Locate every Plasmodium vivax-infected red blood cell.
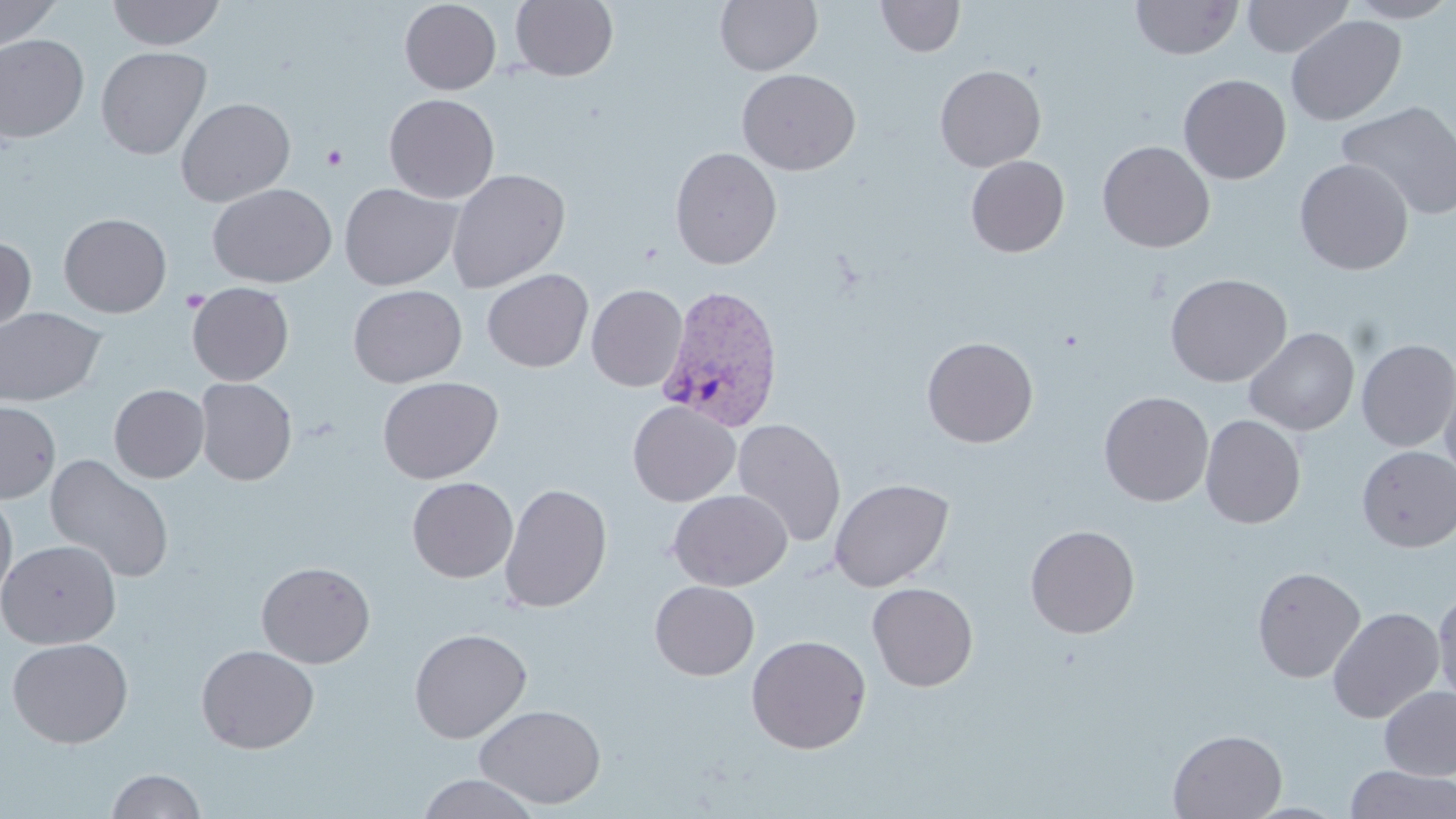
Approximate bounding boxes as named x1/y1/x2/y2 corners in pixels.
Plasmodium vivax-infected red blood cells: (x1=656, y1=284, x2=785, y2=432).

slide-level diagnosis = Plasmodium vivax
stain = May-Grünwald-Giemsa
uninfected red blood cell locations = approximate bounding boxes as named x1/y1/x2/y2 corners in pixels: (x1=0, y1=0, x2=62, y2=50), (x1=106, y1=0, x2=225, y2=50), (x1=399, y1=0, x2=501, y2=95), (x1=510, y1=0, x2=618, y2=81), (x1=715, y1=0, x2=822, y2=76), (x1=876, y1=0, x2=965, y2=58), (x1=1131, y1=0, x2=1243, y2=60), (x1=1241, y1=0, x2=1354, y2=58), (x1=1343, y1=0, x2=1456, y2=23), (x1=1285, y1=14, x2=1406, y2=126), (x1=0, y1=34, x2=90, y2=142), (x1=95, y1=46, x2=212, y2=160), (x1=934, y1=64, x2=1046, y2=172), (x1=736, y1=68, x2=861, y2=175), (x1=1178, y1=74, x2=1291, y2=184), (x1=384, y1=94, x2=500, y2=203), (x1=176, y1=97, x2=296, y2=207), (x1=1337, y1=101, x2=1456, y2=220), (x1=1097, y1=141, x2=1215, y2=253), (x1=670, y1=146, x2=782, y2=269), (x1=965, y1=155, x2=1070, y2=257), (x1=1294, y1=158, x2=1414, y2=275), (x1=446, y1=168, x2=570, y2=292), (x1=339, y1=182, x2=462, y2=290), (x1=207, y1=183, x2=337, y2=287), (x1=59, y1=213, x2=172, y2=317), (x1=0, y1=235, x2=36, y2=338), (x1=481, y1=268, x2=593, y2=372), (x1=1165, y1=273, x2=1292, y2=387), (x1=187, y1=282, x2=294, y2=386), (x1=348, y1=284, x2=467, y2=388), (x1=586, y1=284, x2=687, y2=391), (x1=0, y1=306, x2=106, y2=406), (x1=1244, y1=327, x2=1359, y2=435), (x1=922, y1=336, x2=1038, y2=447), (x1=1356, y1=339, x2=1456, y2=452), (x1=1440, y1=374, x2=1456, y2=489), (x1=377, y1=376, x2=503, y2=484), (x1=195, y1=377, x2=296, y2=485), (x1=109, y1=384, x2=209, y2=483), (x1=1098, y1=391, x2=1214, y2=507), (x1=0, y1=400, x2=61, y2=503), (x1=628, y1=401, x2=740, y2=506), (x1=1200, y1=414, x2=1306, y2=528), (x1=732, y1=418, x2=847, y2=547), (x1=1356, y1=446, x2=1456, y2=552), (x1=44, y1=454, x2=175, y2=584), (x1=407, y1=476, x2=518, y2=582), (x1=829, y1=477, x2=954, y2=592), (x1=499, y1=483, x2=612, y2=613), (x1=668, y1=489, x2=792, y2=591), (x1=0, y1=492, x2=17, y2=607), (x1=1025, y1=524, x2=1140, y2=638), (x1=1, y1=539, x2=121, y2=649), (x1=256, y1=561, x2=375, y2=668), (x1=1251, y1=566, x2=1366, y2=683), (x1=649, y1=580, x2=760, y2=680), (x1=867, y1=582, x2=978, y2=691), (x1=1433, y1=588, x2=1456, y2=711), (x1=1327, y1=606, x2=1445, y2=724), (x1=409, y1=627, x2=531, y2=743), (x1=746, y1=634, x2=871, y2=754), (x1=6, y1=637, x2=133, y2=748), (x1=196, y1=644, x2=319, y2=754), (x1=1379, y1=686, x2=1456, y2=780), (x1=474, y1=704, x2=607, y2=808), (x1=1168, y1=729, x2=1287, y2=818), (x1=1344, y1=765, x2=1456, y2=819), (x1=106, y1=768, x2=206, y2=818), (x1=416, y1=772, x2=541, y2=818), (x1=1242, y1=801, x2=1350, y2=818)
preparation = thin blood film
platelet locations = approximate bounding boxes as named x1/y1/x2/y2 corners in pixels: (x1=322, y1=144, x2=348, y2=170)
magnification = 1000x
modality = light microscopy
image size = 1456×819 pixels
field of view = one of a larger specimen